State which parasite is depicted.
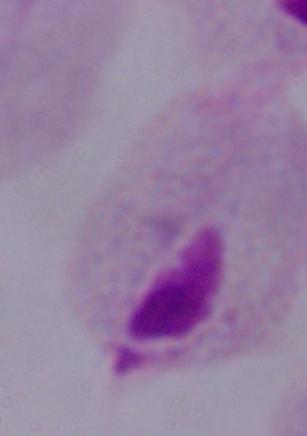

This is a trichomonad.

Summary:
  - Modality: micrograph
  - Magnification: 1000x